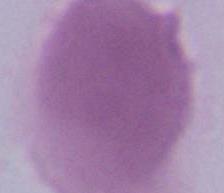
Summary:
  - Identification: erythrocyte
  - Magnification: 1000x
  - Modality: micrograph